Identify the cell.
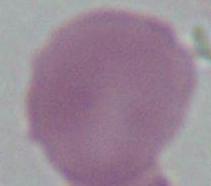
This is an erythrocyte.

Summary:
  - Magnification: 1000x
  - Modality: photomicrograph